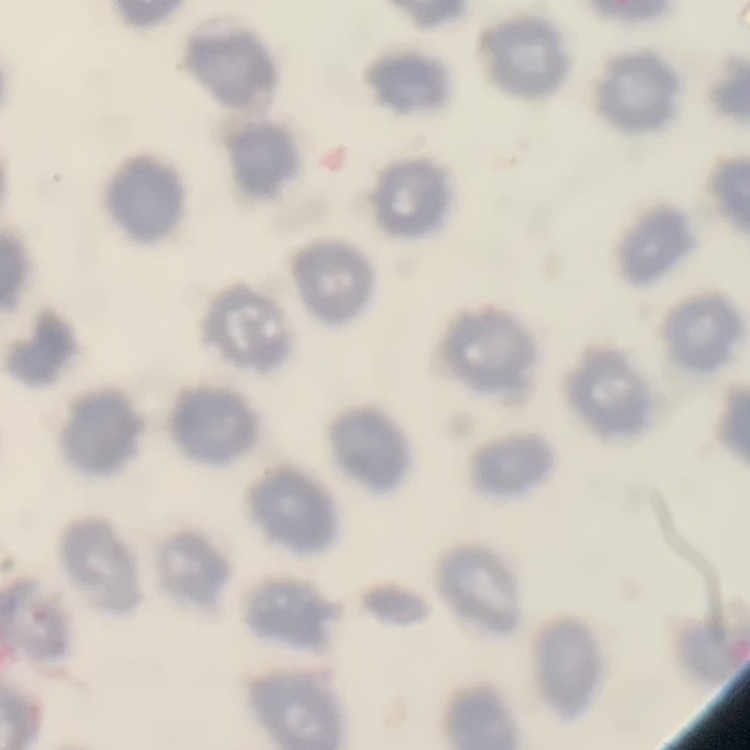
The red blood cells exhibit no rouleaux formation. Field's or Giemsa stain. Square crop of a larger photomicrograph. Thin blood smear.